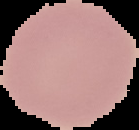 Segmented cell region on a black background. Image is 139×130 pixels. From a thin blood film. Malaria status: uninfected.